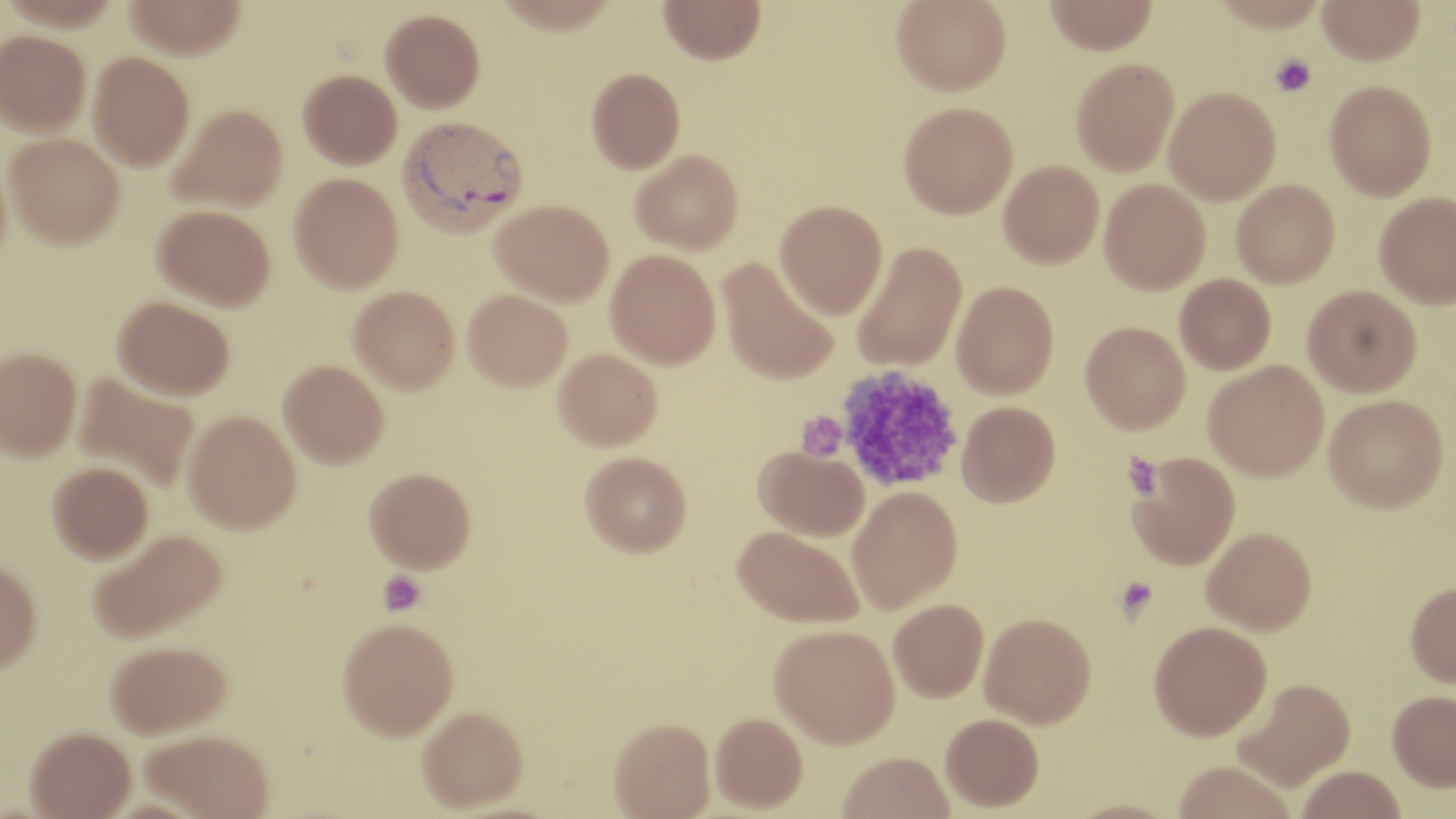
Summary:
  - Coordinate format: approximate bounding boxes as named x1/y1/x2/y2 corners in pixels
  - Platelet locations: (x1=1269, y1=53, x2=1316, y2=97), (x1=837, y1=366, x2=964, y2=494), (x1=795, y1=411, x2=847, y2=462), (x1=1122, y1=452, x2=1163, y2=499), (x1=378, y1=570, x2=425, y2=615), (x1=1115, y1=576, x2=1159, y2=619)
  - Plasmodium vivax-infected red blood cell locations: (x1=397, y1=115, x2=528, y2=237)
  - Uninfected red blood cell locations: (x1=124, y1=0, x2=247, y2=58), (x1=494, y1=0, x2=620, y2=35), (x1=659, y1=0, x2=765, y2=65), (x1=891, y1=0, x2=1012, y2=95), (x1=1044, y1=0, x2=1158, y2=55), (x1=1209, y1=0, x2=1328, y2=32), (x1=1316, y1=0, x2=1425, y2=65), (x1=380, y1=9, x2=485, y2=112), (x1=0, y1=30, x2=91, y2=136), (x1=88, y1=51, x2=195, y2=170), (x1=1070, y1=58, x2=1179, y2=176), (x1=586, y1=67, x2=685, y2=174), (x1=298, y1=69, x2=401, y2=169), (x1=1325, y1=80, x2=1437, y2=200), (x1=1163, y1=87, x2=1281, y2=205), (x1=898, y1=102, x2=1018, y2=218), (x1=167, y1=104, x2=287, y2=211), (x1=4, y1=134, x2=124, y2=249), (x1=630, y1=149, x2=743, y2=254), (x1=998, y1=160, x2=1104, y2=268), (x1=289, y1=172, x2=403, y2=291), (x1=1099, y1=178, x2=1211, y2=294), (x1=1231, y1=179, x2=1340, y2=287), (x1=1374, y1=192, x2=1456, y2=308), (x1=491, y1=199, x2=614, y2=306), (x1=775, y1=199, x2=888, y2=318), (x1=153, y1=204, x2=275, y2=310), (x1=852, y1=241, x2=967, y2=372), (x1=605, y1=249, x2=721, y2=369), (x1=717, y1=257, x2=839, y2=385), (x1=1175, y1=274, x2=1276, y2=374), (x1=951, y1=280, x2=1059, y2=399), (x1=1302, y1=284, x2=1422, y2=396), (x1=348, y1=285, x2=460, y2=392), (x1=462, y1=290, x2=571, y2=391), (x1=113, y1=295, x2=235, y2=400), (x1=1080, y1=321, x2=1190, y2=433), (x1=0, y1=347, x2=81, y2=460), (x1=554, y1=348, x2=662, y2=450), (x1=279, y1=360, x2=389, y2=468), (x1=1203, y1=360, x2=1329, y2=480), (x1=73, y1=374, x2=200, y2=493), (x1=1324, y1=394, x2=1449, y2=512), (x1=956, y1=400, x2=1061, y2=507), (x1=183, y1=410, x2=301, y2=532), (x1=753, y1=445, x2=869, y2=541), (x1=580, y1=451, x2=692, y2=556), (x1=1127, y1=452, x2=1241, y2=570), (x1=47, y1=461, x2=153, y2=562), (x1=365, y1=467, x2=476, y2=572), (x1=847, y1=485, x2=963, y2=613), (x1=732, y1=525, x2=864, y2=628), (x1=1202, y1=527, x2=1317, y2=633), (x1=87, y1=528, x2=226, y2=643), (x1=0, y1=559, x2=42, y2=672), (x1=1405, y1=581, x2=1456, y2=688), (x1=888, y1=598, x2=989, y2=702), (x1=980, y1=612, x2=1096, y2=727), (x1=337, y1=618, x2=458, y2=740), (x1=1149, y1=620, x2=1271, y2=740), (x1=769, y1=624, x2=900, y2=748), (x1=106, y1=640, x2=231, y2=737), (x1=1234, y1=679, x2=1355, y2=791), (x1=1387, y1=689, x2=1456, y2=791), (x1=417, y1=705, x2=528, y2=812), (x1=710, y1=712, x2=807, y2=813), (x1=940, y1=713, x2=1044, y2=812), (x1=608, y1=717, x2=716, y2=819), (x1=25, y1=726, x2=135, y2=819), (x1=140, y1=730, x2=274, y2=818), (x1=837, y1=752, x2=954, y2=819), (x1=1171, y1=763, x2=1296, y2=819), (x1=1295, y1=765, x2=1407, y2=819)
  - Slide-level diagnosis: Plasmodium vivax
  - Magnification: 1000x
  - Stain: May-Grünwald-Giemsa
  - Field of view: single
  - Image size: 1456×819 pixels
  - Preparation: thin blood film
  - Modality: light microscopy